Identify the blood parasite species.
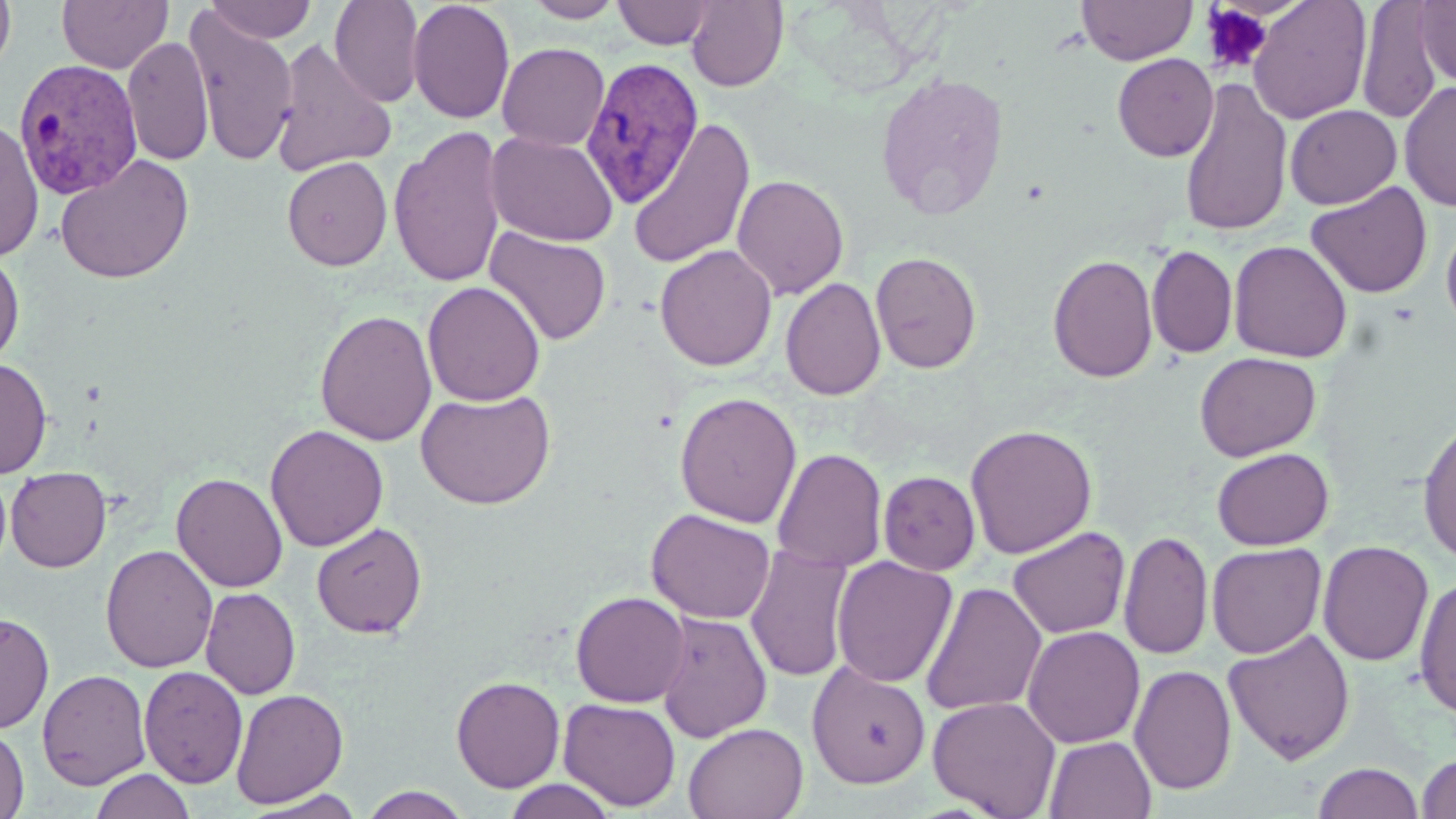

Plasmodium vivax.

Approximate bounding boxes as (x1,y1)-(x2,y2) corner pairs in pixels. Uninfected red blood cell locations: (0,0)-(16,77), (57,0)-(173,74), (329,0)-(424,106), (407,0)-(515,124), (522,0)-(627,22), (685,0)-(788,91), (1076,0)-(1197,66), (1248,0)-(1372,124), (1414,0)-(1456,86), (205,1)-(316,43), (613,1)-(716,49), (1356,1)-(1443,123), (183,7)-(299,167), (122,35)-(213,167), (271,38)-(396,177), (497,42)-(610,151), (1112,53)-(1219,162), (874,72)-(1010,219), (1179,78)-(1292,237), (1399,80)-(1456,212), (1285,104)-(1401,209), (627,118)-(755,269), (0,119)-(43,261), (389,125)-(507,288), (485,131)-(619,247), (282,149)-(504,276), (55,153)-(194,285), (282,156)-(392,271), (731,173)-(849,300), (1306,181)-(1432,299), (1441,215)-(1456,339), (484,226)-(612,346), (1229,240)-(1352,363), (654,244)-(777,371), (1147,244)-(1238,358), (0,248)-(24,370), (870,251)-(982,374), (1047,254)-(1158,383), (780,277)-(886,401), (423,281)-(546,406), (315,309)-(437,446), (1194,351)-(1320,461), (0,357)-(53,478), (416,390)-(555,509), (675,392)-(802,528), (1417,417)-(1456,566), (965,423)-(1097,559), (265,424)-(388,552), (1212,447)-(1334,550), (773,448)-(887,573), (5,466)-(111,572), (878,470)-(980,575), (171,472)-(288,593), (646,508)-(775,624), (311,521)-(427,638), (1007,526)-(1130,639), (1119,530)-(1213,660), (1317,540)-(1433,667), (1207,542)-(1326,659), (745,543)-(854,683), (100,544)-(219,673), (831,556)-(957,688), (1414,575)-(1456,720), (920,581)-(1047,717), (200,587)-(301,699), (570,591)-(690,707), (0,611)-(54,733), (655,611)-(773,743), (1023,625)-(1145,748), (1223,628)-(1355,764), (807,662)-(931,788), (1129,664)-(1236,795), (139,666)-(248,788), (37,668)-(151,790), (450,675)-(565,792), (231,688)-(348,808), (927,696)-(1062,818), (559,698)-(680,810), (683,722)-(808,819), (0,723)-(29,819), (1044,735)-(1156,819), (1417,753)-(1456,818), (1312,762)-(1425,819), (91,768)-(196,819), (500,778)-(621,819), (359,786)-(472,819), (244,789)-(366,818). Platelet locations: (1201,4)-(1273,74). Plasmodium vivax-infected red blood cell locations: (580,56)-(704,209), (14,59)-(144,199). May-Grünwald-Giemsa-stained preparation. Image is 1456×819 pixels. Thin blood smear. Captured at 1000x magnification. Single field of view. Optical microscopy.